Locate every Plasmodium parasite and every leukocyte.
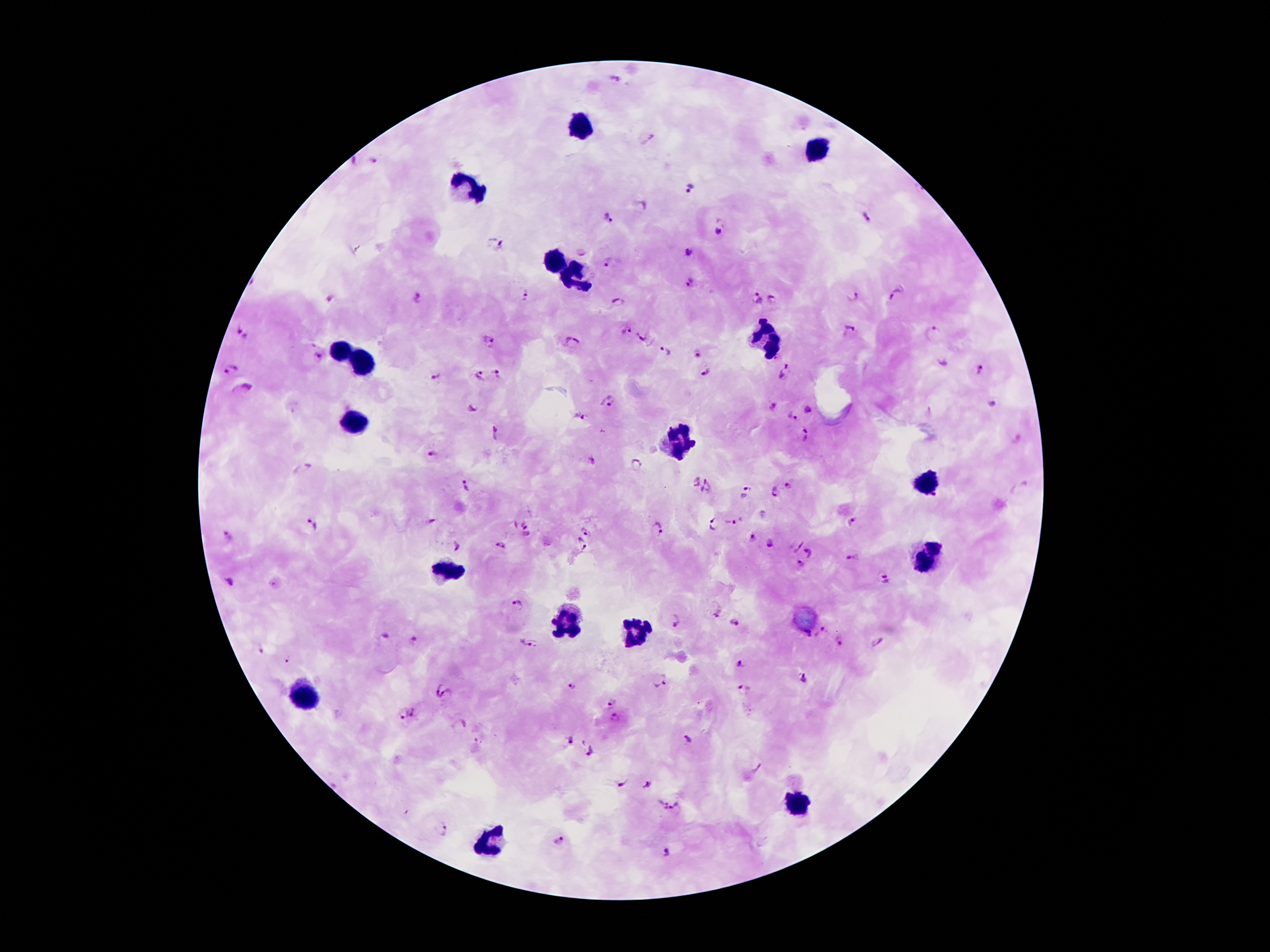
Approximate centers as [x, y] in pixels.
Plasmodium parasites: [614, 78], [648, 138], [374, 161], [353, 162], [690, 187], [641, 207], [609, 218], [866, 219], [719, 233], [495, 242], [689, 255], [609, 263], [690, 284], [526, 294], [897, 295], [854, 297], [756, 298], [774, 299], [331, 300], [419, 300], [618, 301], [238, 330], [626, 330], [850, 330], [933, 334], [247, 338], [640, 338], [489, 342], [572, 343], [666, 351], [695, 354], [319, 356], [943, 364], [230, 369], [981, 370], [788, 372], [704, 373], [496, 375], [480, 376], [434, 377], [243, 390], [608, 402], [991, 403], [471, 407], [772, 407], [808, 411], [583, 418], [790, 419], [498, 433], [807, 436], [434, 453], [592, 459], [636, 466], [303, 469], [694, 481], [467, 487], [709, 487], [789, 487], [772, 492], [744, 493], [431, 521], [733, 522], [854, 522], [313, 524], [714, 524], [657, 528], [527, 531], [586, 531], [751, 537], [229, 539], [770, 544], [500, 545], [580, 545], [796, 545], [457, 547], [811, 552], [855, 559], [801, 565], [883, 578], [229, 581], [517, 605], [714, 612], [676, 620], [734, 622], [822, 632], [385, 636], [414, 640], [839, 642], [527, 643], [880, 643], [260, 649], [287, 659], [740, 666], [804, 679], [659, 681], [574, 685], [436, 686], [744, 689], [447, 695], [611, 703], [401, 713], [413, 713], [615, 719], [459, 724], [570, 740], [690, 741], [591, 751], [620, 783], [648, 785], [660, 805], [677, 811], [442, 830], [558, 841], [664, 853].
Leukocytes: [579, 126], [818, 149], [466, 187], [555, 264], [576, 279], [767, 338], [340, 351], [360, 363], [355, 424], [678, 443], [927, 486], [927, 559], [444, 570], [564, 624], [635, 631], [306, 699], [795, 803], [489, 841].

stain = Giemsa
magnification = 100x
field of view = single
preparation = thick peripheral-blood smear
patient malaria status = infected with Plasmodium falciparum
capture = smartphone through the microscope eyepiece
image size = 1270×952 pixels